Locate every Plasmodium parasite.
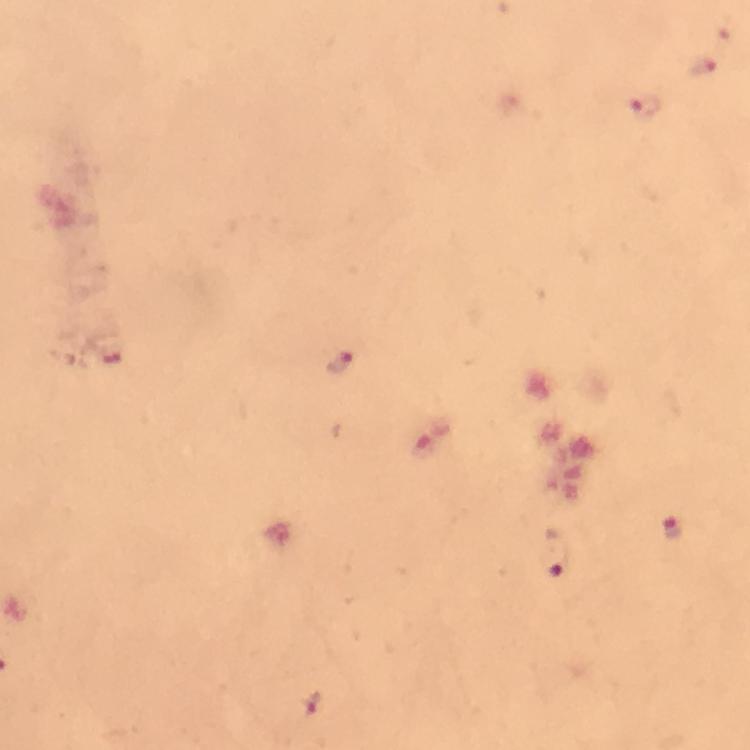

Approximate centers as [x, y] in pixels.
Plasmodium parasites: [703, 66], [647, 107], [340, 360], [672, 530], [555, 555], [311, 702].

Summary:
  - Cropped from: a single field of view
  - Capture: smartphone photograph through a microscope
  - Stain: Giemsa
  - Magnification: 100x
  - Immersion oil: applied
  - Preparation: thick blood smear
  - Context: from a diagnostic examination for malaria
  - Image size: 750×750 pixels